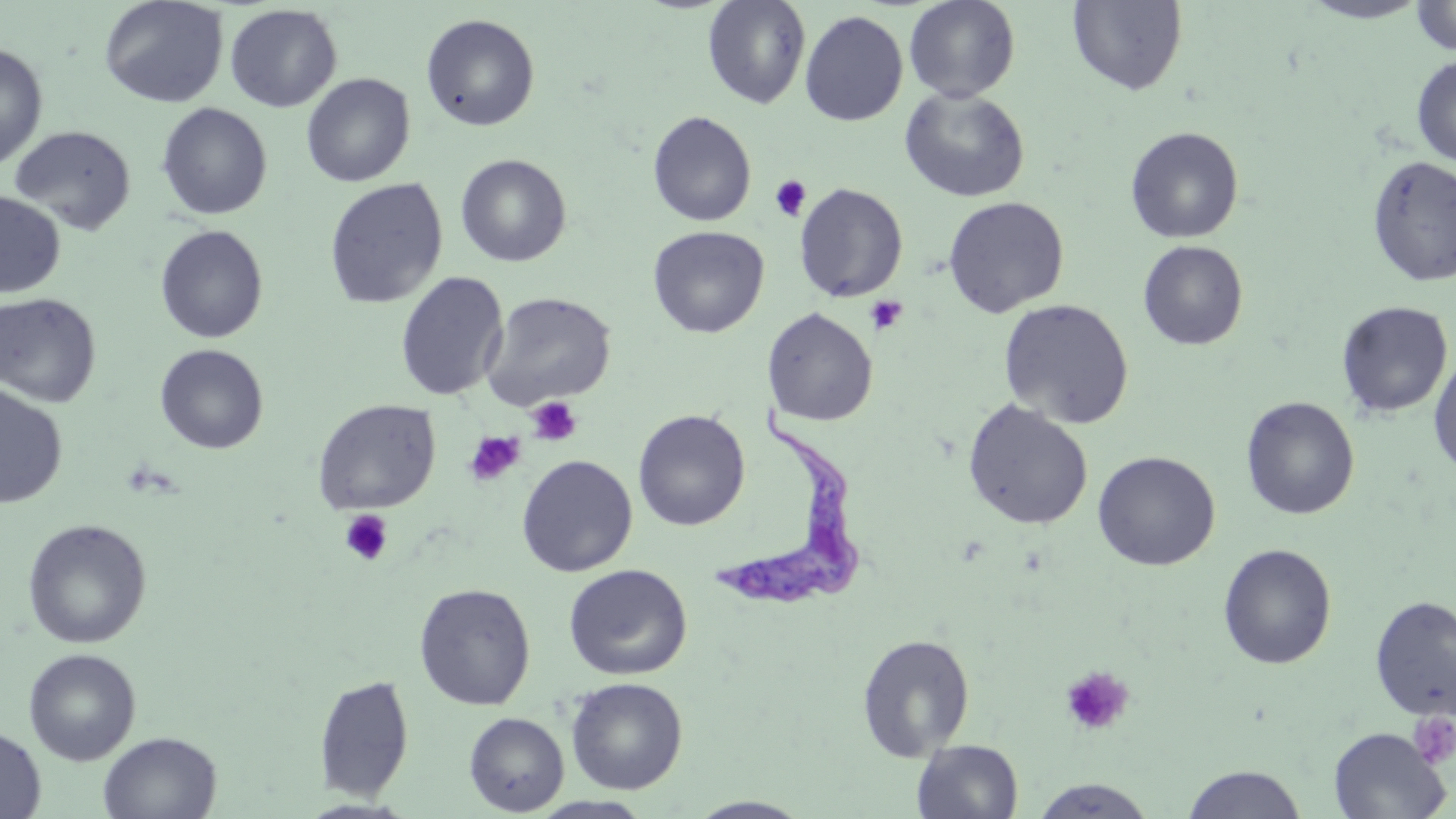
Approximate bounding boxes as (x1, y1, x2, y2) in pixels. Trypanosoma brucei locations: (709, 400, 867, 612). Uninfected red blood cell locations: (100, 0, 228, 108), (702, 0, 812, 110), (904, 0, 1020, 103), (1299, 0, 1432, 23), (1068, 1, 1187, 95), (1411, 1, 1456, 56), (225, 4, 342, 112), (800, 11, 908, 126), (420, 13, 540, 132), (0, 42, 49, 171), (1411, 55, 1456, 166), (301, 73, 415, 187), (899, 87, 1030, 202), (156, 102, 272, 220), (647, 110, 757, 227), (9, 125, 136, 234), (1125, 126, 1245, 244), (456, 154, 571, 267), (1366, 154, 1456, 288), (324, 178, 448, 309), (794, 182, 908, 302), (0, 192, 65, 297), (943, 196, 1069, 318), (155, 225, 269, 343), (648, 226, 769, 338), (1138, 240, 1248, 351), (395, 271, 509, 401), (480, 291, 616, 410), (0, 292, 102, 407), (998, 298, 1135, 429), (1336, 301, 1453, 419), (762, 307, 878, 426), (155, 343, 269, 454), (1428, 350, 1456, 477), (0, 383, 68, 509), (1240, 396, 1360, 520), (312, 399, 441, 515), (962, 400, 1093, 530), (632, 409, 750, 531), (1093, 451, 1220, 571), (516, 454, 638, 577), (22, 518, 152, 649), (1217, 543, 1337, 670), (563, 564, 692, 680), (414, 582, 536, 710), (1369, 594, 1456, 720), (857, 632, 975, 760), (23, 648, 141, 765), (314, 675, 415, 800), (565, 677, 688, 795), (463, 712, 569, 815), (0, 725, 46, 819), (1328, 727, 1450, 818), (98, 731, 222, 819), (912, 740, 1023, 819), (1181, 764, 1309, 819), (1029, 779, 1158, 818), (529, 795, 655, 818), (687, 797, 814, 818). Platelet locations: (770, 175, 811, 222), (865, 295, 908, 334), (526, 396, 583, 446), (464, 431, 525, 487), (340, 509, 394, 566), (1060, 666, 1134, 737), (1409, 712, 1456, 770). Slide-level diagnosis: Trypanosoma brucei. Image is 1456×819 pixels. May-Grünwald-Giemsa stain. Thin blood smear. 1000x magnification. Optical microscopy. Single field of view.